Locate every Plasmodium ovale-infected red blood cell.
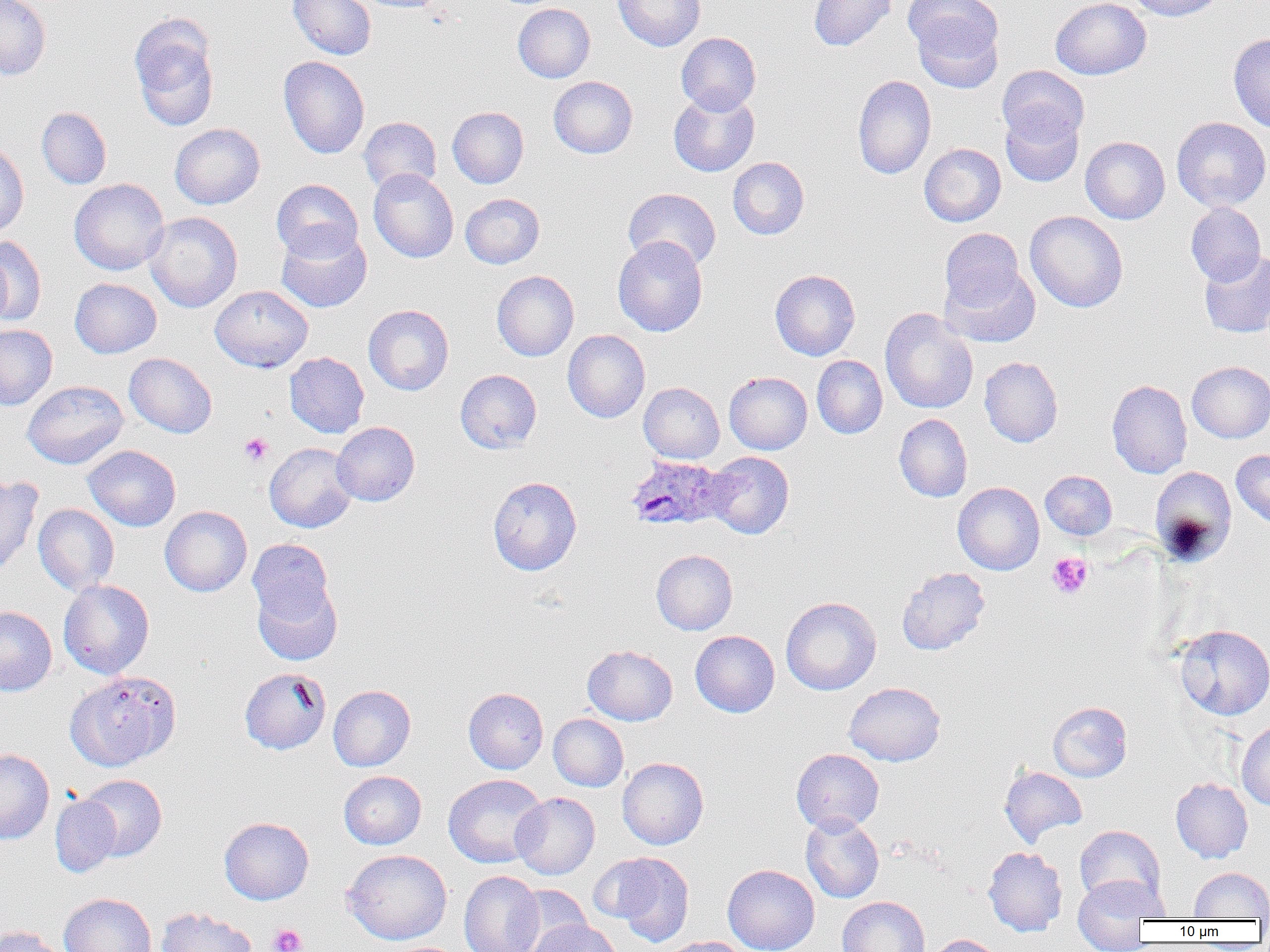

Approximate bounding boxes as (x1, y1, x2, y2) in pixels.
Plasmodium ovale-infected red blood cells: (625, 455, 732, 531).

slide_level_diagnosis: Plasmodium ovale
preparation: thin blood smear
field_of_view: single
platelet_locations: 'approximate bounding boxes as (x1, y1, x2, y2) in pixels: (239, 432, 273, 466), (1047, 552, 1093, 599), (269, 924, 307, 952)'
image_size: 1270×952 pixels
uninfected_red_blood_cell_locations: 'approximate bounding boxes as (x1, y1, x2, y2) in pixels: (0, 0, 51, 80), (288, 0, 377, 60), (351, 0, 451, 13), (613, 0, 705, 51), (809, 0, 896, 51), (1050, 0, 1151, 80), (1125, 0, 1226, 21), (905, 1, 1005, 89), (513, 3, 595, 83), (129, 15, 220, 131), (676, 32, 761, 114), (1228, 33, 1270, 132), (278, 56, 369, 158), (997, 65, 1090, 147), (852, 74, 936, 179), (548, 76, 638, 158), (668, 89, 760, 177), (447, 106, 529, 188), (37, 107, 111, 189), (1000, 107, 1084, 187), (359, 117, 441, 194), (1171, 117, 1270, 212), (169, 123, 265, 209), (1080, 136, 1170, 224), (0, 140, 29, 237), (919, 143, 1006, 226), (728, 157, 809, 239), (368, 169, 458, 262), (69, 178, 169, 275), (271, 179, 363, 262), (622, 187, 721, 271), (460, 193, 545, 269), (1185, 202, 1266, 285), (1025, 210, 1128, 312), (144, 212, 242, 312), (276, 226, 372, 313), (939, 228, 1025, 311), (1, 235, 46, 326), (613, 236, 708, 336), (0, 249, 12, 331), (1199, 251, 1270, 338), (940, 262, 1041, 348), (770, 269, 860, 360), (491, 270, 579, 361), (70, 278, 162, 358), (210, 285, 313, 372), (363, 304, 454, 395), (880, 308, 978, 414), (0, 325, 57, 410), (563, 329, 650, 422), (284, 352, 369, 438), (124, 353, 217, 438), (812, 355, 887, 438), (979, 356, 1063, 447), (1187, 361, 1270, 443), (455, 369, 542, 453), (724, 371, 812, 454), (1106, 379, 1192, 478), (23, 380, 129, 469), (639, 382, 724, 464), (894, 414, 972, 502), (331, 422, 419, 506), (265, 442, 358, 532), (83, 445, 181, 531), (1231, 449, 1270, 530), (704, 451, 794, 539), (1150, 466, 1237, 565), (1040, 470, 1117, 540), (0, 476, 42, 578), (488, 476, 582, 575), (953, 482, 1045, 575), (34, 504, 119, 595), (160, 506, 252, 596), (247, 538, 335, 626), (651, 549, 737, 635), (897, 567, 990, 655), (253, 578, 343, 666), (58, 579, 155, 679), (781, 597, 881, 695), (0, 606, 57, 696), (1173, 624, 1270, 720), (690, 630, 779, 717), (582, 645, 678, 725), (239, 667, 330, 755), (65, 670, 181, 771), (845, 682, 946, 766), (328, 685, 416, 771), (464, 688, 548, 773), (1048, 702, 1131, 782), (549, 713, 629, 791), (1236, 720, 1270, 811), (791, 748, 884, 834), (0, 749, 54, 844), (617, 757, 709, 849), (999, 766, 1088, 845), (338, 771, 426, 849), (79, 774, 167, 861), (443, 774, 547, 868), (1170, 777, 1253, 863), (511, 792, 600, 879), (50, 794, 121, 878), (801, 814, 884, 902), (218, 817, 313, 905), (1075, 825, 1165, 909), (983, 846, 1067, 936), (341, 849, 452, 945), (604, 853, 695, 945), (722, 864, 820, 952), (1189, 867, 1270, 919), (459, 871, 543, 952), (1073, 874, 1168, 945), (511, 887, 593, 951), (59, 893, 156, 952), (837, 896, 929, 952), (155, 906, 257, 952), (529, 919, 621, 952), (0, 925, 67, 952), (925, 934, 1005, 952), (661, 937, 752, 952)'
magnification: 1000x
modality: optical microscopy